Report the malaria status of this cell.
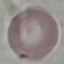

It is uninfected.

stain = Giemsa
capture = smartphone through the microscope eyepiece
image type = automatically extracted cell patch, resized to 64 × 64 pixels
preparation = thin blood smear